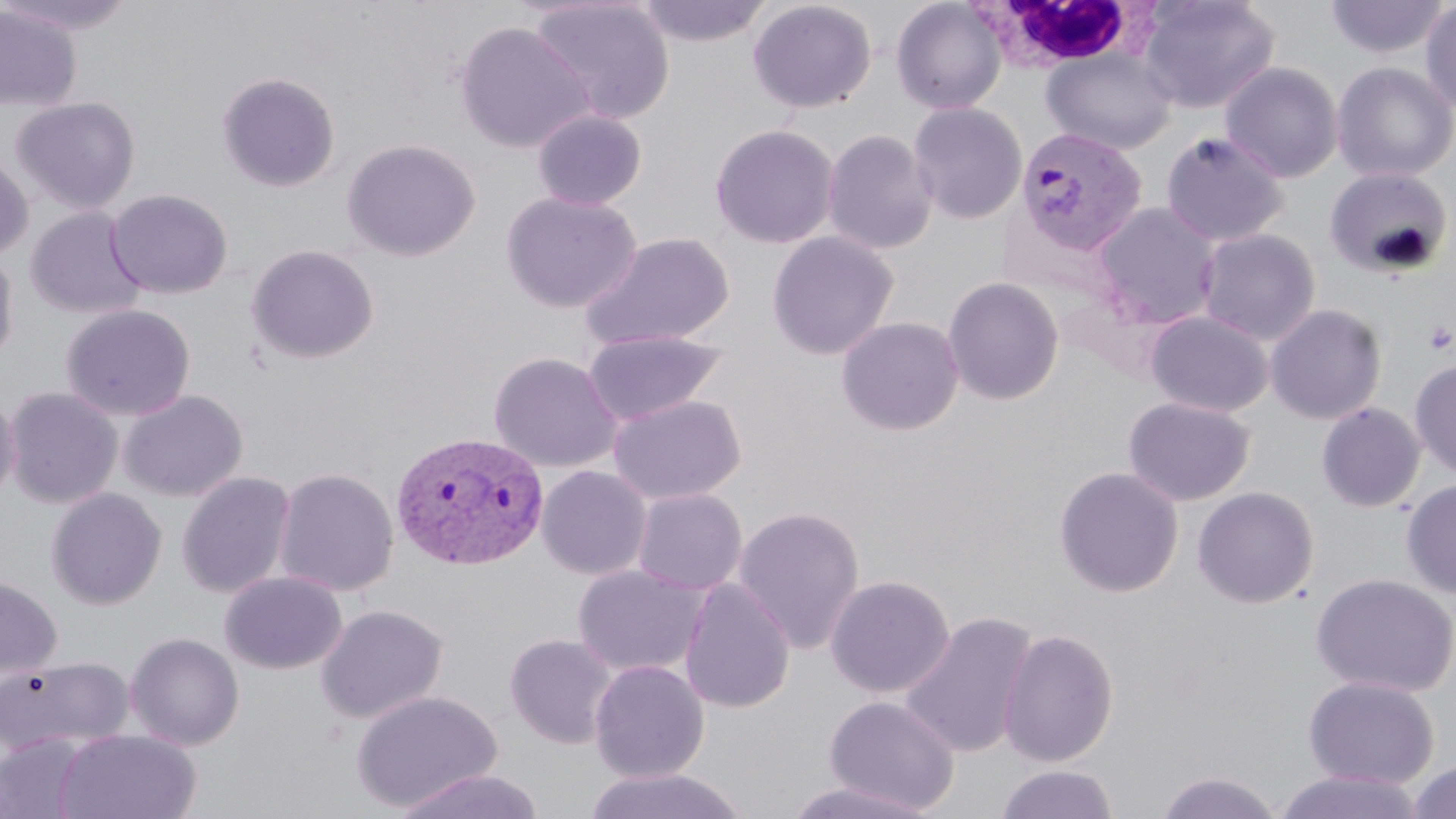
slide-level diagnosis = Plasmodium vivax
uninfected red blood cell locations = approximate bounding boxes as (x1,y1)-(x2,y2) corner pairs in pixels: (0,0)-(139,35), (528,0)-(675,125), (635,0)-(771,47), (748,0)-(877,114), (890,0)-(1007,115), (1137,0)-(1279,114), (1324,0)-(1450,60), (1420,3)-(1456,116), (0,4)-(82,112), (454,21)-(592,153), (1041,47)-(1177,154), (1331,61)-(1456,183), (1220,62)-(1343,182), (217,72)-(341,193), (11,97)-(141,214), (908,101)-(1028,225), (532,109)-(648,211), (710,123)-(840,249), (822,128)-(938,255), (1159,129)-(1291,247), (342,138)-(480,262), (0,151)-(33,261), (1323,167)-(1454,279), (106,189)-(233,299), (501,190)-(641,313), (1091,202)-(1222,329), (25,207)-(148,321), (1196,227)-(1321,344), (579,231)-(735,351), (766,231)-(900,360), (245,244)-(379,365), (0,247)-(19,364), (942,277)-(1065,405), (1265,303)-(1387,425), (60,304)-(195,422), (1146,310)-(1274,417), (836,316)-(964,436), (581,330)-(730,426), (488,351)-(623,472), (1410,360)-(1456,480), (4,387)-(124,509), (0,388)-(20,506), (118,390)-(247,502), (607,394)-(746,504), (1123,396)-(1256,506), (1316,401)-(1426,512), (536,465)-(652,580), (1054,465)-(1184,598), (273,466)-(399,597), (177,470)-(297,598), (1401,479)-(1456,598), (1192,486)-(1320,608), (46,487)-(166,610), (631,488)-(748,596), (733,505)-(866,654), (571,564)-(709,678), (220,571)-(347,674), (1310,572)-(1456,697), (825,574)-(955,698), (0,575)-(62,681), (679,578)-(796,713), (316,604)-(448,724), (899,611)-(1038,759), (998,627)-(1120,767), (126,632)-(245,751), (504,633)-(618,749), (0,654)-(136,757), (589,659)-(710,782), (1302,675)-(1440,790), (350,689)-(503,812), (824,694)-(961,814), (54,728)-(201,819), (0,734)-(91,819), (1405,758)-(1456,819), (995,765)-(1120,819), (584,766)-(747,819), (389,769)-(545,819), (1272,769)-(1428,819), (1153,770)-(1285,818), (781,779)-(937,819)
white blood cell locations = approximate bounding boxes as (x1,y1)-(x2,y2) corner pairs in pixels: (975,2)-(1156,72)
preparation = thin blood smear
stain = May-Grünwald-Giemsa
modality = optical microscopy
magnification = 1000x
field of view = one of a larger specimen
Plasmodium vivax-infected red blood cell locations = approximate bounding boxes as (x1,y1)-(x2,y2) corner pairs in pixels: (1015,126)-(1148,256), (389,430)-(549,571)
image size = 1456×819 pixels
platelet locations = approximate bounding boxes as (x1,y1)-(x2,y2) corner pairs in pixels: (1423,318)-(1455,356)